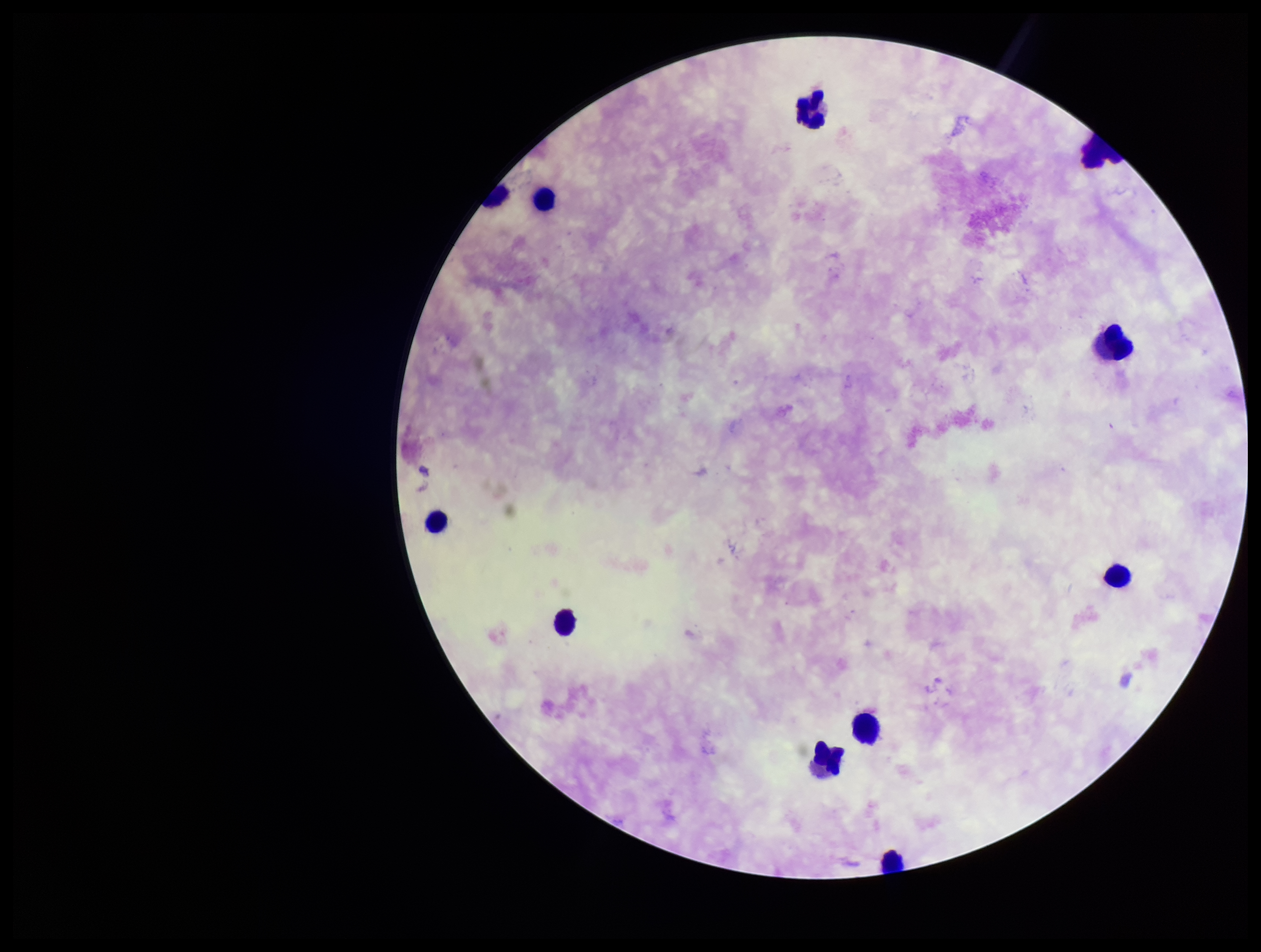
Summary:
  - Patient malaria status: negative
  - Stain: Giemsa
  - Field of view: single
  - Capture: smartphone photograph through the microscope eyepiece
  - Image size: 1261×952 pixels
  - Parasite count: 0
  - Leukocyte count: 11
  - Plasmodium parasites: none identified
  - Preparation: thick